Locate every blood parasite and identify its species.
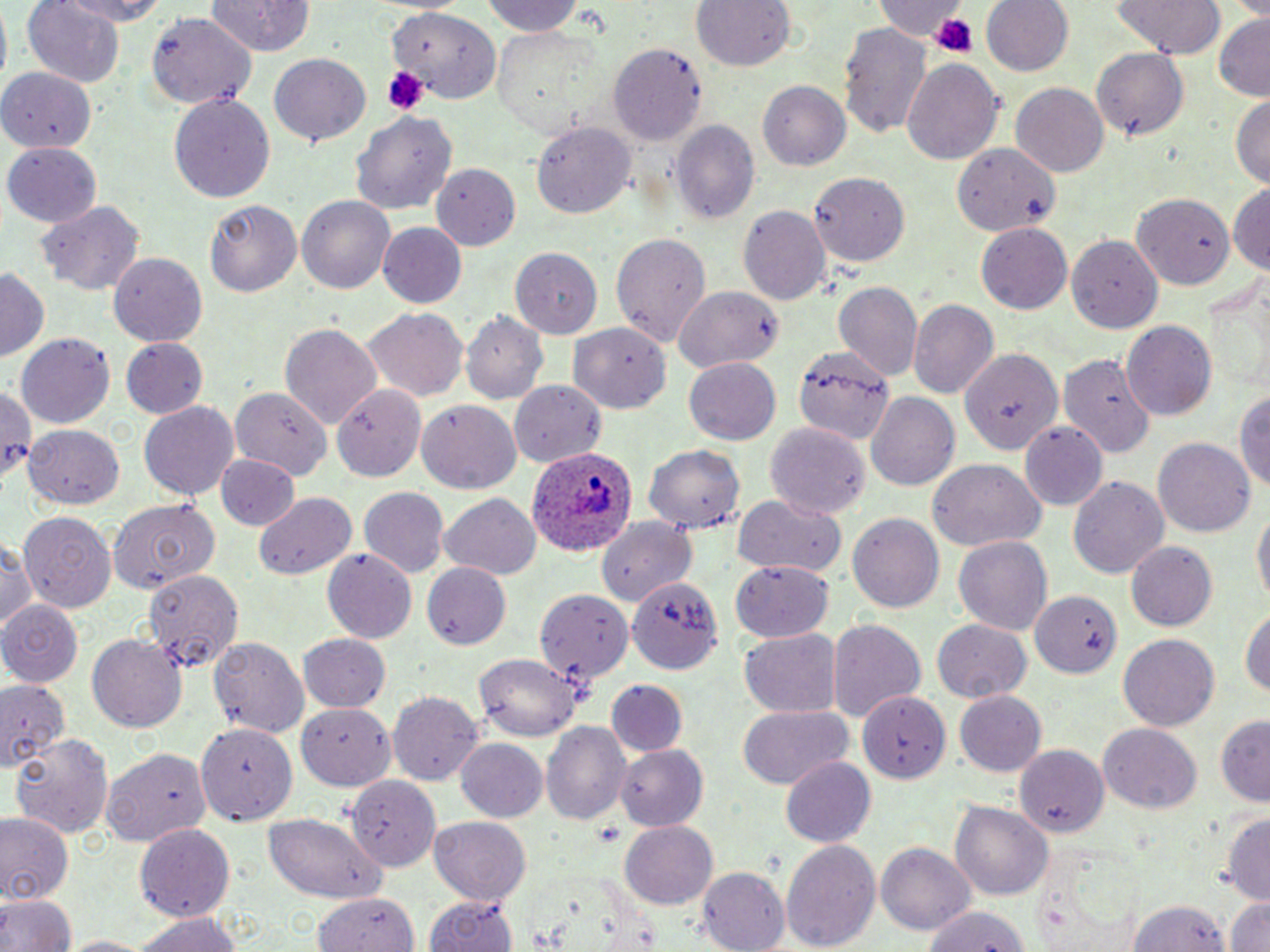

Approximate bounding boxes as named x1/y1/x2/y2 corners in pixels.
Plasmodium ovale-infected red blood cells: (x1=526, y1=449, x2=638, y2=560).
No Plasmodium falciparum, Plasmodium malariae, Plasmodium vivax, Babesia divergens, or Trypanosoma brucei observed.

Summary:
  - Uninfected red blood cell locations: (x1=50, y1=0, x2=169, y2=26), (x1=204, y1=0, x2=314, y2=56), (x1=484, y1=0, x2=590, y2=37), (x1=691, y1=0, x2=794, y2=73), (x1=979, y1=0, x2=1073, y2=78), (x1=1110, y1=0, x2=1227, y2=60), (x1=24, y1=1, x2=124, y2=87), (x1=874, y1=1, x2=970, y2=41), (x1=390, y1=7, x2=497, y2=106), (x1=147, y1=11, x2=255, y2=110), (x1=1212, y1=16, x2=1269, y2=101), (x1=840, y1=24, x2=932, y2=140), (x1=489, y1=27, x2=602, y2=138), (x1=609, y1=46, x2=706, y2=145), (x1=1091, y1=48, x2=1190, y2=141), (x1=267, y1=52, x2=372, y2=147), (x1=900, y1=57, x2=1005, y2=164), (x1=0, y1=63, x2=99, y2=148), (x1=758, y1=80, x2=850, y2=170), (x1=1012, y1=82, x2=1110, y2=177), (x1=1231, y1=92, x2=1270, y2=189), (x1=168, y1=93, x2=278, y2=203), (x1=354, y1=110, x2=456, y2=214), (x1=673, y1=118, x2=760, y2=224), (x1=533, y1=121, x2=634, y2=219), (x1=5, y1=142, x2=103, y2=226), (x1=950, y1=144, x2=1061, y2=234), (x1=432, y1=164, x2=518, y2=248), (x1=809, y1=172, x2=911, y2=265), (x1=1230, y1=185, x2=1269, y2=276), (x1=296, y1=194, x2=396, y2=295), (x1=1131, y1=194, x2=1233, y2=288), (x1=204, y1=197, x2=306, y2=296), (x1=34, y1=199, x2=145, y2=297), (x1=739, y1=204, x2=830, y2=305), (x1=376, y1=223, x2=467, y2=309), (x1=976, y1=223, x2=1072, y2=315), (x1=610, y1=231, x2=711, y2=348), (x1=1066, y1=234, x2=1164, y2=333), (x1=512, y1=247, x2=601, y2=338), (x1=108, y1=252, x2=208, y2=345), (x1=0, y1=269, x2=49, y2=363), (x1=835, y1=282, x2=924, y2=382), (x1=674, y1=288, x2=782, y2=374), (x1=909, y1=300, x2=998, y2=398), (x1=360, y1=305, x2=468, y2=402), (x1=462, y1=312, x2=549, y2=405), (x1=1121, y1=321, x2=1216, y2=420), (x1=279, y1=322, x2=382, y2=431), (x1=573, y1=324, x2=670, y2=414), (x1=15, y1=332, x2=116, y2=428), (x1=120, y1=338, x2=208, y2=420), (x1=793, y1=347, x2=893, y2=442), (x1=960, y1=347, x2=1061, y2=455), (x1=1059, y1=351, x2=1155, y2=455), (x1=683, y1=359, x2=780, y2=444), (x1=509, y1=380, x2=609, y2=465), (x1=333, y1=382, x2=427, y2=483), (x1=1235, y1=382, x2=1270, y2=499), (x1=0, y1=384, x2=42, y2=484), (x1=232, y1=388, x2=330, y2=486), (x1=866, y1=392, x2=959, y2=493), (x1=416, y1=401, x2=521, y2=493), (x1=138, y1=402, x2=240, y2=500), (x1=767, y1=423, x2=870, y2=520), (x1=1019, y1=423, x2=1107, y2=509), (x1=24, y1=424, x2=125, y2=507), (x1=1153, y1=438, x2=1257, y2=539), (x1=643, y1=444, x2=746, y2=535), (x1=217, y1=454, x2=296, y2=529), (x1=926, y1=458, x2=1047, y2=552), (x1=1068, y1=475, x2=1169, y2=578), (x1=358, y1=486, x2=449, y2=579), (x1=254, y1=490, x2=357, y2=581), (x1=438, y1=494, x2=541, y2=579), (x1=730, y1=494, x2=849, y2=580), (x1=109, y1=500, x2=219, y2=596), (x1=1251, y1=504, x2=1269, y2=609), (x1=848, y1=510, x2=944, y2=611), (x1=19, y1=512, x2=116, y2=614), (x1=597, y1=515, x2=695, y2=611), (x1=1, y1=538, x2=40, y2=637), (x1=954, y1=538, x2=1051, y2=634), (x1=1125, y1=542, x2=1217, y2=632), (x1=323, y1=547, x2=418, y2=642), (x1=730, y1=561, x2=834, y2=642), (x1=423, y1=562, x2=509, y2=648), (x1=143, y1=567, x2=245, y2=675), (x1=632, y1=574, x2=733, y2=676), (x1=528, y1=582, x2=638, y2=690), (x1=1026, y1=588, x2=1125, y2=680), (x1=1, y1=598, x2=82, y2=684), (x1=1239, y1=604, x2=1269, y2=703), (x1=827, y1=618, x2=926, y2=719), (x1=930, y1=620, x2=1032, y2=703), (x1=86, y1=631, x2=186, y2=730), (x1=739, y1=631, x2=840, y2=716), (x1=298, y1=633, x2=389, y2=710), (x1=1119, y1=633, x2=1219, y2=728), (x1=208, y1=635, x2=309, y2=738), (x1=474, y1=654, x2=581, y2=739), (x1=0, y1=679, x2=71, y2=772), (x1=606, y1=680, x2=688, y2=756), (x1=856, y1=689, x2=951, y2=784), (x1=389, y1=692, x2=484, y2=786), (x1=954, y1=692, x2=1046, y2=775), (x1=296, y1=703, x2=391, y2=788), (x1=738, y1=706, x2=853, y2=789), (x1=1214, y1=710, x2=1270, y2=804), (x1=544, y1=722, x2=630, y2=825), (x1=199, y1=724, x2=299, y2=823), (x1=1099, y1=724, x2=1202, y2=813), (x1=9, y1=730, x2=112, y2=840), (x1=455, y1=738, x2=547, y2=822), (x1=1016, y1=742, x2=1113, y2=838), (x1=613, y1=744, x2=707, y2=831), (x1=104, y1=746, x2=210, y2=846), (x1=781, y1=757, x2=876, y2=849), (x1=347, y1=768, x2=441, y2=873), (x1=952, y1=802, x2=1051, y2=901), (x1=1221, y1=811, x2=1270, y2=903), (x1=0, y1=812, x2=72, y2=904), (x1=263, y1=813, x2=388, y2=901), (x1=428, y1=817, x2=532, y2=904), (x1=620, y1=820, x2=718, y2=911), (x1=134, y1=823, x2=236, y2=920), (x1=782, y1=837, x2=881, y2=952), (x1=877, y1=843, x2=976, y2=935), (x1=700, y1=866, x2=791, y2=952), (x1=310, y1=890, x2=416, y2=952), (x1=1, y1=892, x2=75, y2=952), (x1=422, y1=893, x2=521, y2=952), (x1=1127, y1=896, x2=1233, y2=950), (x1=1227, y1=897, x2=1270, y2=952), (x1=918, y1=905, x2=1033, y2=952), (x1=129, y1=907, x2=244, y2=952), (x1=52, y1=933, x2=162, y2=951)
  - Platelet locations: (x1=932, y1=13, x2=979, y2=56), (x1=385, y1=66, x2=426, y2=116), (x1=595, y1=822, x2=621, y2=845)
  - Slide-level diagnosis: Plasmodium ovale
  - Magnification: 1000x
  - Field of view: one of a larger specimen
  - Image size: 1270×952 pixels
  - Preparation: thin blood smear
  - Stain: May-Grünwald-Giemsa
  - Modality: optical microscopy